State the preparation type.
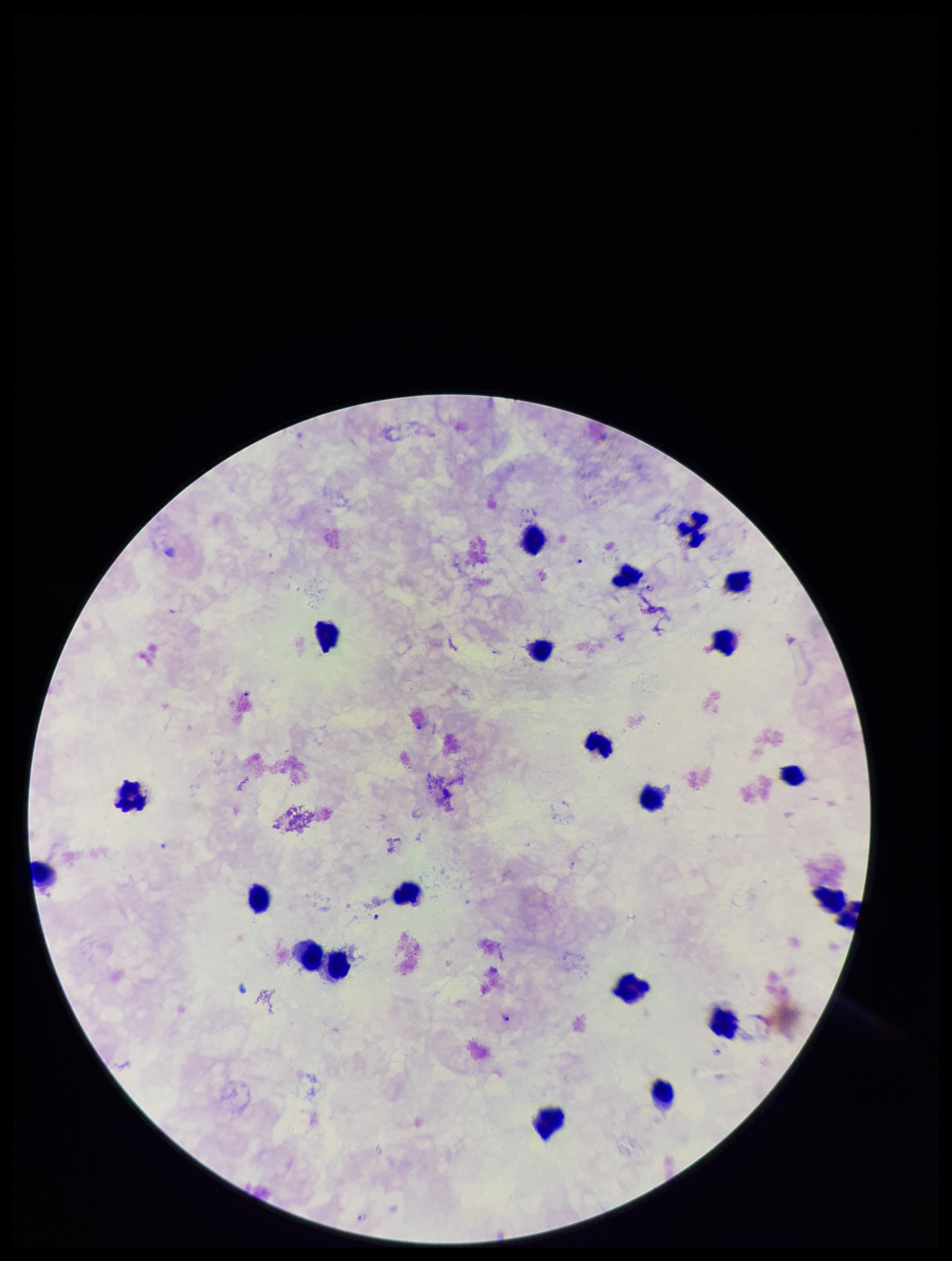
A thick smear.

Patient malaria status: positive. Parasite count: 3. Smartphone photograph taken through the eyepiece of a microscope. Leukocyte count: 22. Stained with Giemsa. Species reported for this patient: Plasmodium falciparum. Plasmodium parasites: seen. One field from this slide. Image is 952×1261 pixels.